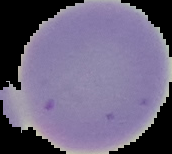 Image is 172×154 pixels. From a thin blood smear. The area outside the segmented cell region is set to black. Malaria status: uninfected.